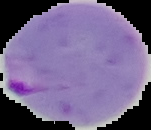
image size = 151×130 pixels
malaria status = parasitized
image type = cell region segmented out of the field of view; surrounding area masked to black
preparation = thin blood film